Locate every Plasmodium parasite and identify its life-cycle stage.
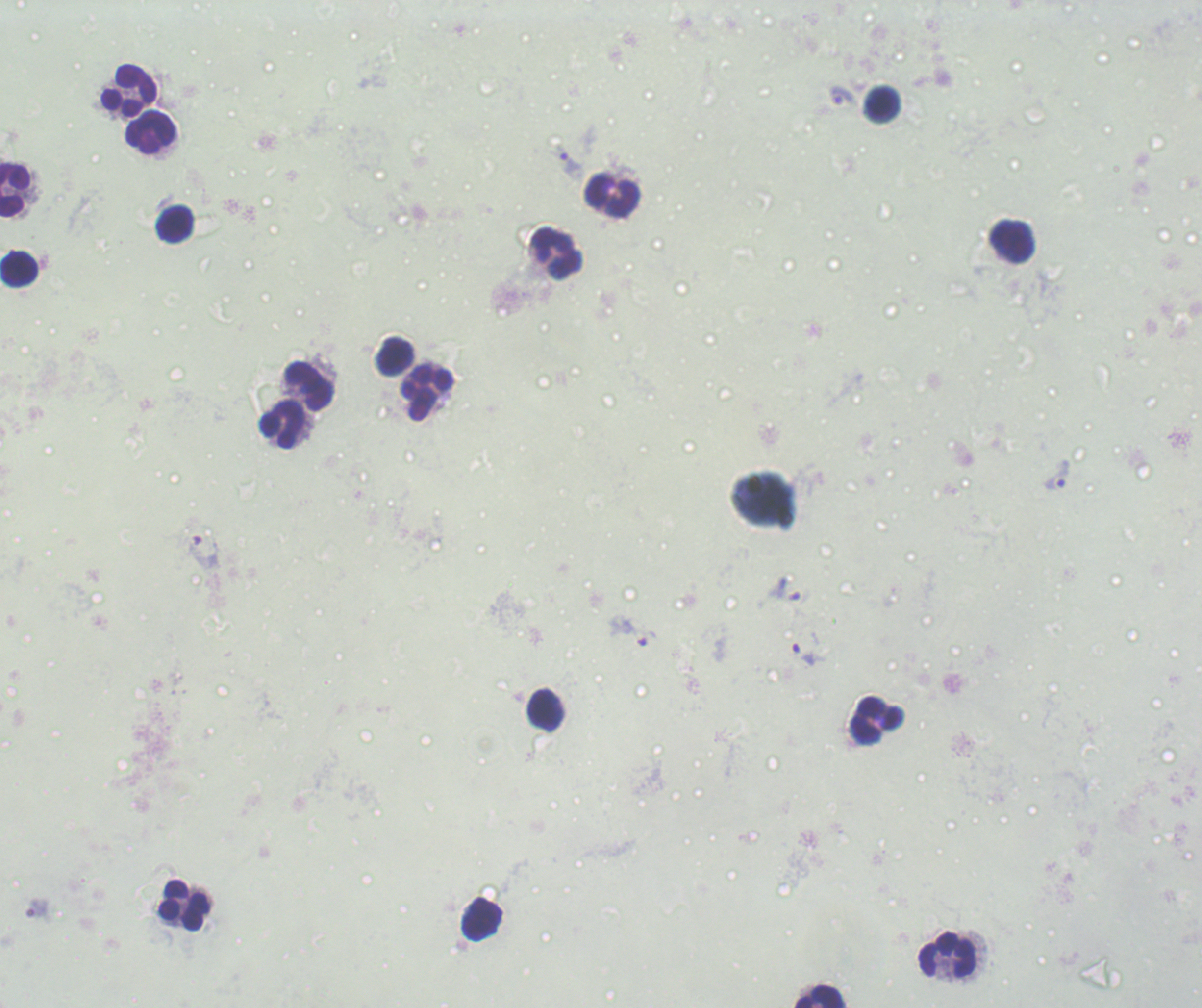

Approximate object centers, in pixels from the top-left corner.
Trophozoites: (x=841, y=96), (x=570, y=163), (x=1058, y=475), (x=205, y=552), (x=787, y=590), (x=631, y=631), (x=804, y=654), (x=38, y=910).
No schizont or gametocyte forms observed.

coordinate format = approximate object centers, in pixels from the top-left corner
leukocyte locations = (x=129, y=91), (x=882, y=104), (x=150, y=132), (x=14, y=189), (x=612, y=196), (x=175, y=224), (x=1012, y=240), (x=558, y=254), (x=18, y=269), (x=395, y=355), (x=308, y=385), (x=426, y=393), (x=281, y=424), (x=546, y=710), (x=877, y=721), (x=184, y=906), (x=483, y=919), (x=947, y=955), (x=819, y=996)
context = previously used in an actual diagnosis
background quality = unsatisfactory
stain = Romanowsky
preparation = thick blood smear
image size = 1202×1008 pixels
field of view = one from this slide
magnification = 100x